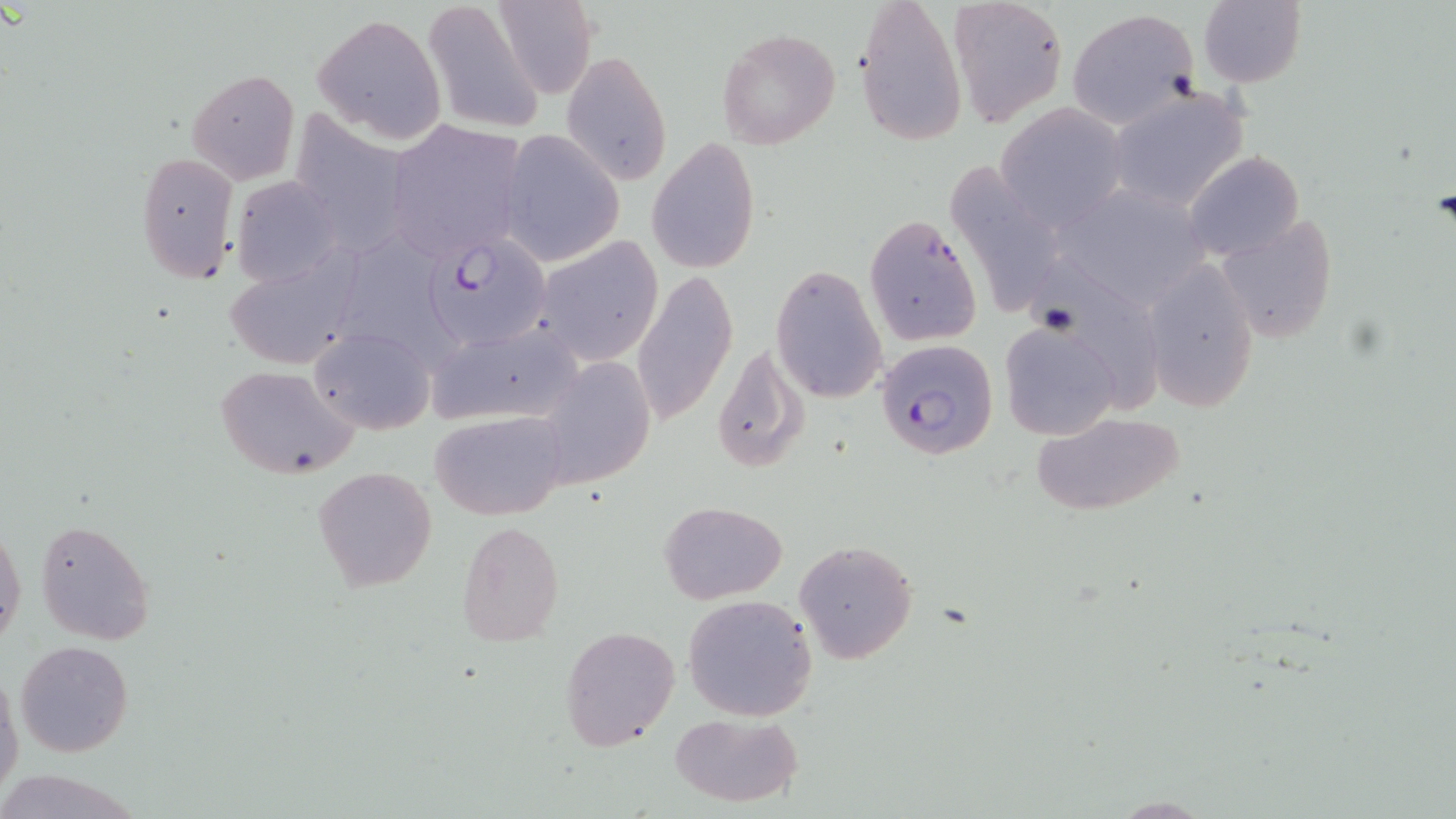

{
  "slide_level_diagnosis": "Plasmodium falciparum",
  "field_of_view": "one of a larger specimen",
  "modality": "optical microscopy",
  "preparation": "thin blood smear",
  "stain": "May-Grünwald-Giemsa",
  "plasmodium_falciparum_infected_red_blood_cell_locations": "approximate bounding boxes as (x1, y1, x2, y2) in pixels: (426, 232, 550, 350), (874, 338, 998, 460)",
  "image_size": "1456×819 pixels",
  "uninfected_red_blood_cell_locations": "approximate bounding boxes as (x1, y1, x2, y2) in pixels: (491, 0, 599, 100), (855, 0, 967, 146), (945, 0, 1068, 126), (422, 1, 544, 135), (1197, 2, 1306, 87), (1070, 8, 1199, 126), (312, 15, 447, 144), (716, 26, 840, 151), (562, 53, 671, 186), (186, 68, 300, 185), (1111, 88, 1248, 212), (994, 103, 1129, 230), (304, 111, 403, 257), (386, 119, 525, 266), (501, 130, 625, 267), (645, 140, 761, 273), (1184, 150, 1304, 263), (135, 151, 240, 283), (943, 164, 1067, 319), (231, 178, 342, 285), (1213, 213, 1339, 344), (864, 214, 984, 349), (535, 236, 665, 366), (357, 237, 454, 369), (223, 253, 359, 371), (1142, 260, 1260, 412), (771, 264, 889, 402), (631, 269, 736, 427), (997, 319, 1122, 441), (427, 322, 582, 425), (309, 326, 435, 437), (711, 343, 807, 476), (535, 356, 657, 490), (214, 363, 357, 479), (430, 409, 570, 521), (1029, 413, 1185, 517), (313, 465, 437, 592), (658, 500, 787, 604), (36, 519, 155, 643), (0, 520, 25, 653), (457, 520, 565, 647), (795, 539, 918, 666), (683, 594, 818, 722), (559, 624, 681, 754), (14, 639, 134, 758), (0, 672, 23, 803), (668, 711, 804, 808)",
  "magnification": "1000x"
}